Point out each Plasmodium parasite.
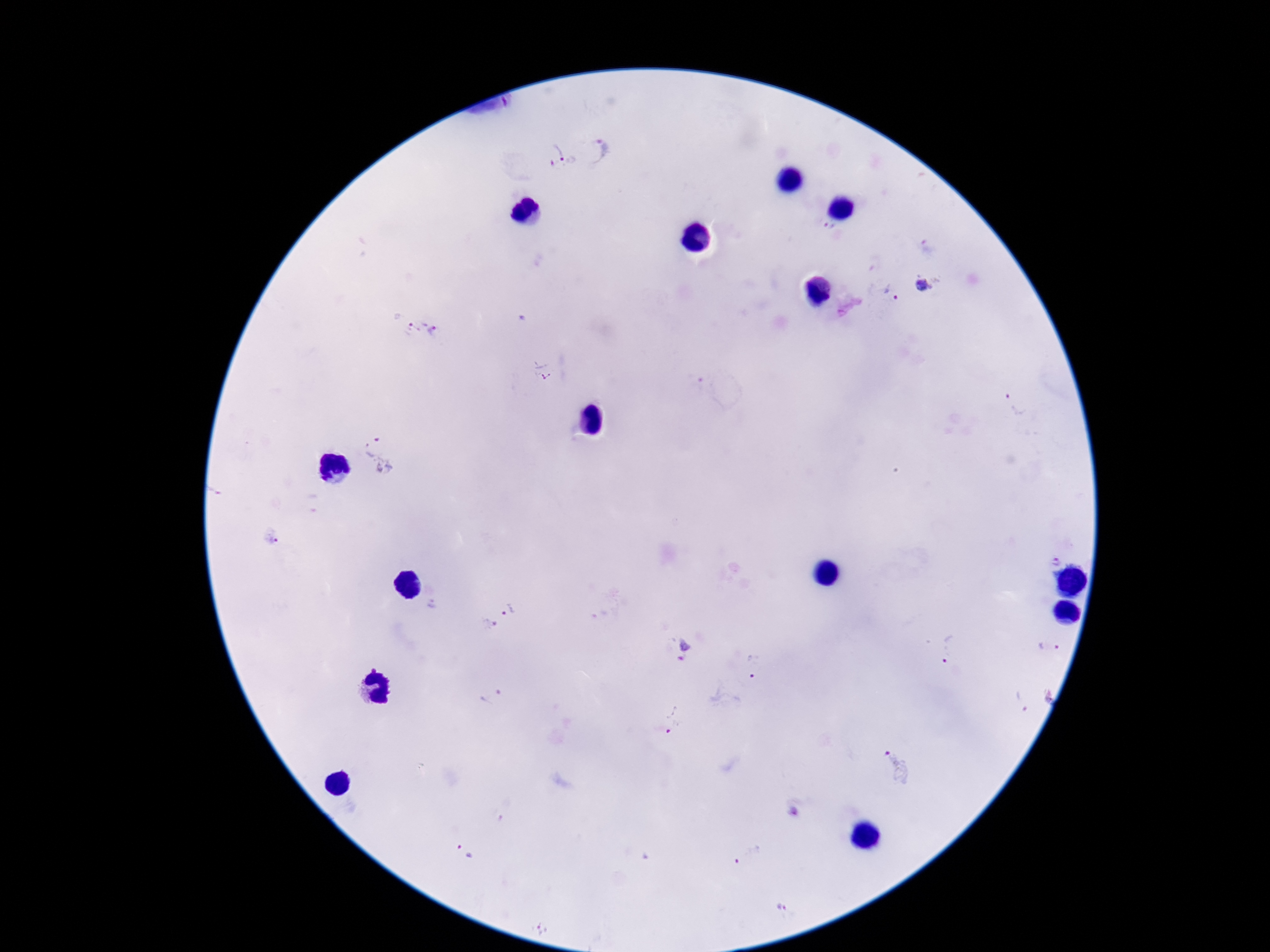
Approximate centers as [x, y] in pixels.
Plasmodium parasites: [602, 151], [563, 157], [829, 227], [924, 284], [891, 293], [414, 326], [436, 331], [542, 370], [1014, 404], [382, 452], [273, 536], [1054, 558], [509, 609], [488, 624], [1049, 647], [685, 651], [949, 651], [755, 667], [492, 697], [1023, 701], [675, 720], [898, 768], [795, 812], [466, 852], [747, 855], [781, 907], [542, 927].

field of view = single
patient malaria status = infected
preparation = thick blood smear
stain = Giemsa
image size = 1270×952 pixels
magnification = 100x
capture = smartphone camera through the microscope eyepiece